Comment on the morphology of the red blood cells.
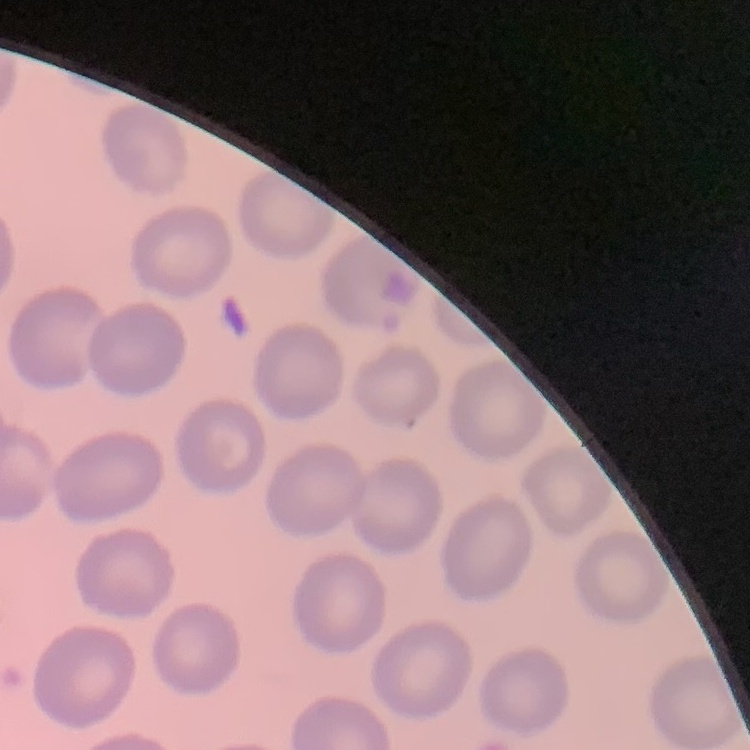
They show no rouleaux formation.

preparation = thin blood film
stain = Field's or Giemsa
image type = one tile cut from a larger photomicrograph